Outline each uninfected red blood cell.
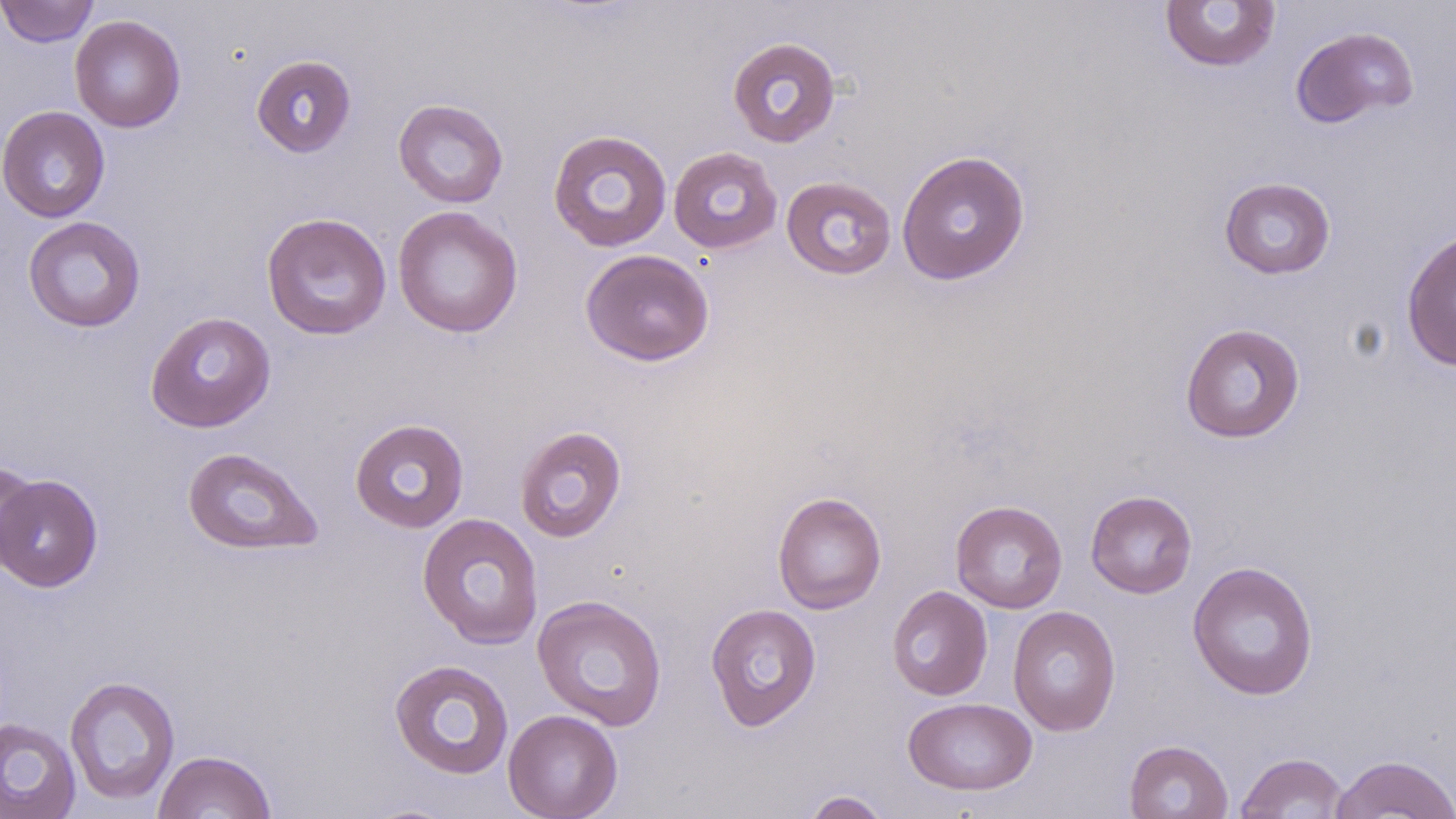
Approximate bounding boxes as named x1/y1/x2/y2 corners in pixels.
Uninfected red blood cells: (x1=0, y1=0, x2=99, y2=47), (x1=1159, y1=1, x2=1282, y2=73), (x1=69, y1=14, x2=186, y2=132), (x1=1290, y1=26, x2=1419, y2=129), (x1=726, y1=36, x2=842, y2=148), (x1=251, y1=53, x2=357, y2=158), (x1=393, y1=98, x2=509, y2=208), (x1=0, y1=105, x2=111, y2=223), (x1=547, y1=129, x2=673, y2=252), (x1=668, y1=146, x2=782, y2=254), (x1=895, y1=149, x2=1031, y2=286), (x1=781, y1=176, x2=897, y2=281), (x1=1219, y1=176, x2=1336, y2=280), (x1=392, y1=205, x2=524, y2=338), (x1=261, y1=212, x2=392, y2=341), (x1=22, y1=216, x2=146, y2=333), (x1=1401, y1=228, x2=1456, y2=372), (x1=579, y1=248, x2=715, y2=367), (x1=145, y1=311, x2=276, y2=433), (x1=1179, y1=322, x2=1306, y2=444), (x1=350, y1=418, x2=469, y2=533), (x1=514, y1=425, x2=627, y2=542), (x1=181, y1=446, x2=324, y2=556), (x1=0, y1=463, x2=39, y2=569), (x1=1, y1=475, x2=103, y2=592), (x1=1085, y1=489, x2=1197, y2=599), (x1=772, y1=491, x2=887, y2=614), (x1=950, y1=499, x2=1068, y2=613), (x1=417, y1=512, x2=544, y2=649), (x1=1187, y1=560, x2=1319, y2=701), (x1=887, y1=585, x2=993, y2=701), (x1=531, y1=594, x2=668, y2=731), (x1=705, y1=603, x2=821, y2=732), (x1=1007, y1=605, x2=1121, y2=737), (x1=388, y1=658, x2=514, y2=780), (x1=64, y1=675, x2=181, y2=806), (x1=902, y1=697, x2=1037, y2=796), (x1=503, y1=709, x2=623, y2=819), (x1=0, y1=717, x2=81, y2=819), (x1=1124, y1=740, x2=1233, y2=819), (x1=153, y1=750, x2=277, y2=819), (x1=1235, y1=751, x2=1350, y2=818), (x1=1329, y1=753, x2=1456, y2=819), (x1=801, y1=790, x2=892, y2=819).

Slide-level diagnosis: no evidence of blood parasites. Light microscopy. Single field of view. Thin blood smear. Image is 1456×819 pixels. May-Grünwald-Giemsa stain. 1000x magnification.